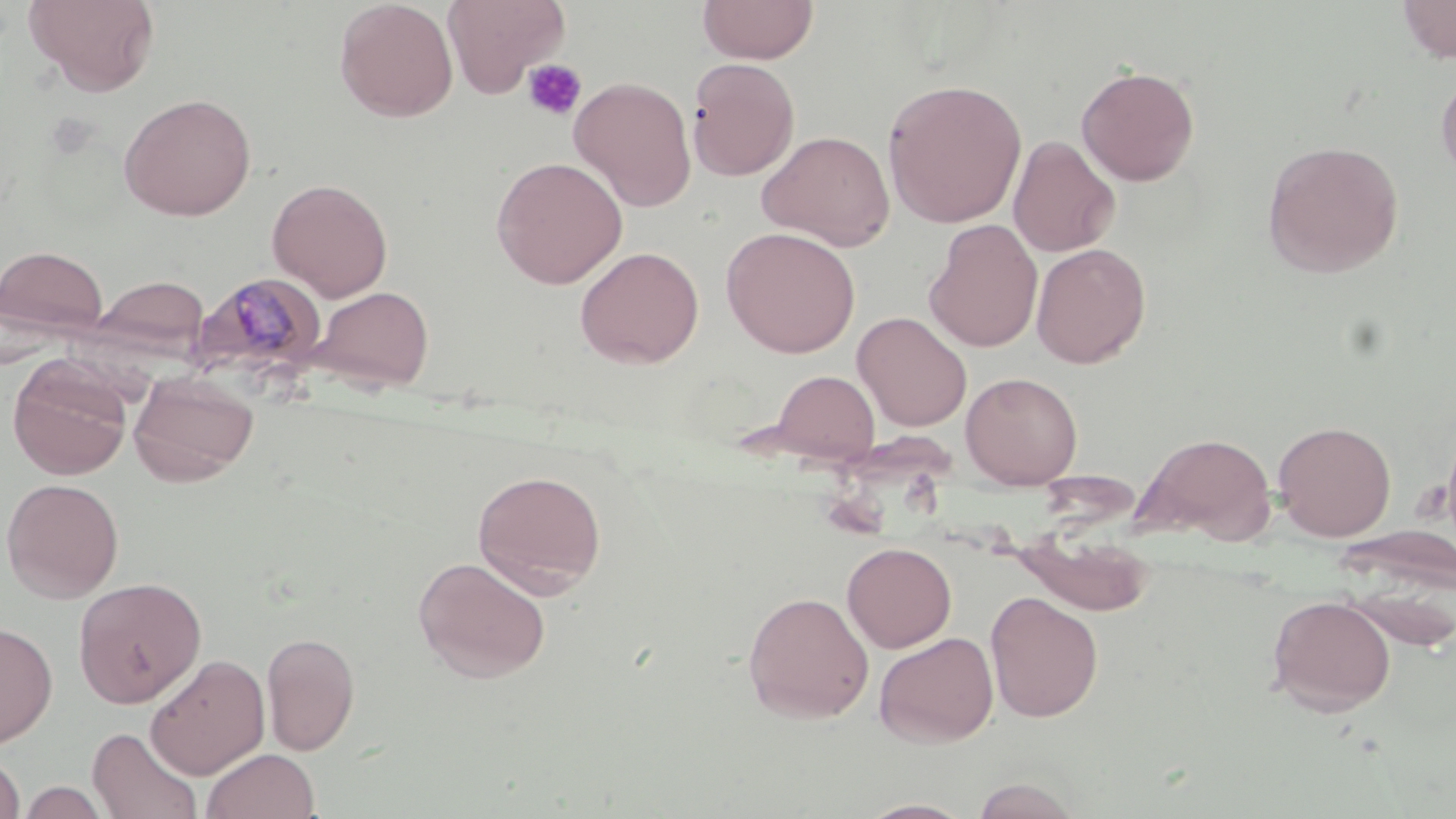
slide-level diagnosis = Plasmodium malariae
modality = light microscopy
field of view = one of a larger specimen
stain = May-Grünwald-Giemsa
image size = 1456×819 pixels
magnification = 1000x
platelet locations = approximate bounding boxes as (x1,y1)-(x2,y2) corner pairs in pixels: (522,59)-(587,121)
uninfected red blood cell locations = approximate bounding boxes as (x1,y1)-(x2,y2) corner pairs in pixels: (24,0)-(161,97), (334,0)-(458,122), (442,0)-(569,98), (697,0)-(819,64), (1397,0)-(1456,64), (686,57)-(800,181), (1076,64)-(1200,186), (1436,69)-(1456,182), (569,76)-(697,211), (882,78)-(1027,228), (118,92)-(257,221), (756,130)-(895,251), (1008,134)-(1121,258), (1262,139)-(1404,277), (491,156)-(628,289), (267,178)-(393,301), (924,219)-(1043,353), (721,226)-(860,358), (1031,243)-(1151,368), (0,244)-(109,342), (574,246)-(704,368), (89,274)-(210,360), (312,285)-(435,391), (853,311)-(972,431), (8,358)-(132,480), (769,369)-(880,464), (960,371)-(1083,489), (128,373)-(258,486), (1272,420)-(1396,541), (1133,431)-(1277,543), (472,469)-(607,596), (1,477)-(124,602), (1008,531)-(1157,616), (842,542)-(956,652), (413,556)-(550,684), (73,576)-(207,708), (742,590)-(874,724), (985,591)-(1104,723), (1266,595)-(1396,716), (0,621)-(58,747), (262,631)-(361,756), (873,631)-(999,748), (145,653)-(270,779), (88,726)-(202,818), (201,748)-(320,819), (0,751)-(26,818), (969,777)-(1083,818), (17,778)-(111,818), (856,798)-(978,818)
Plasmodium malariae-infected red blood cell locations = approximate bounding boxes as (x1,y1)-(x2,y2) corner pairs in pixels: (193,271)-(328,382)
preparation = thin blood film